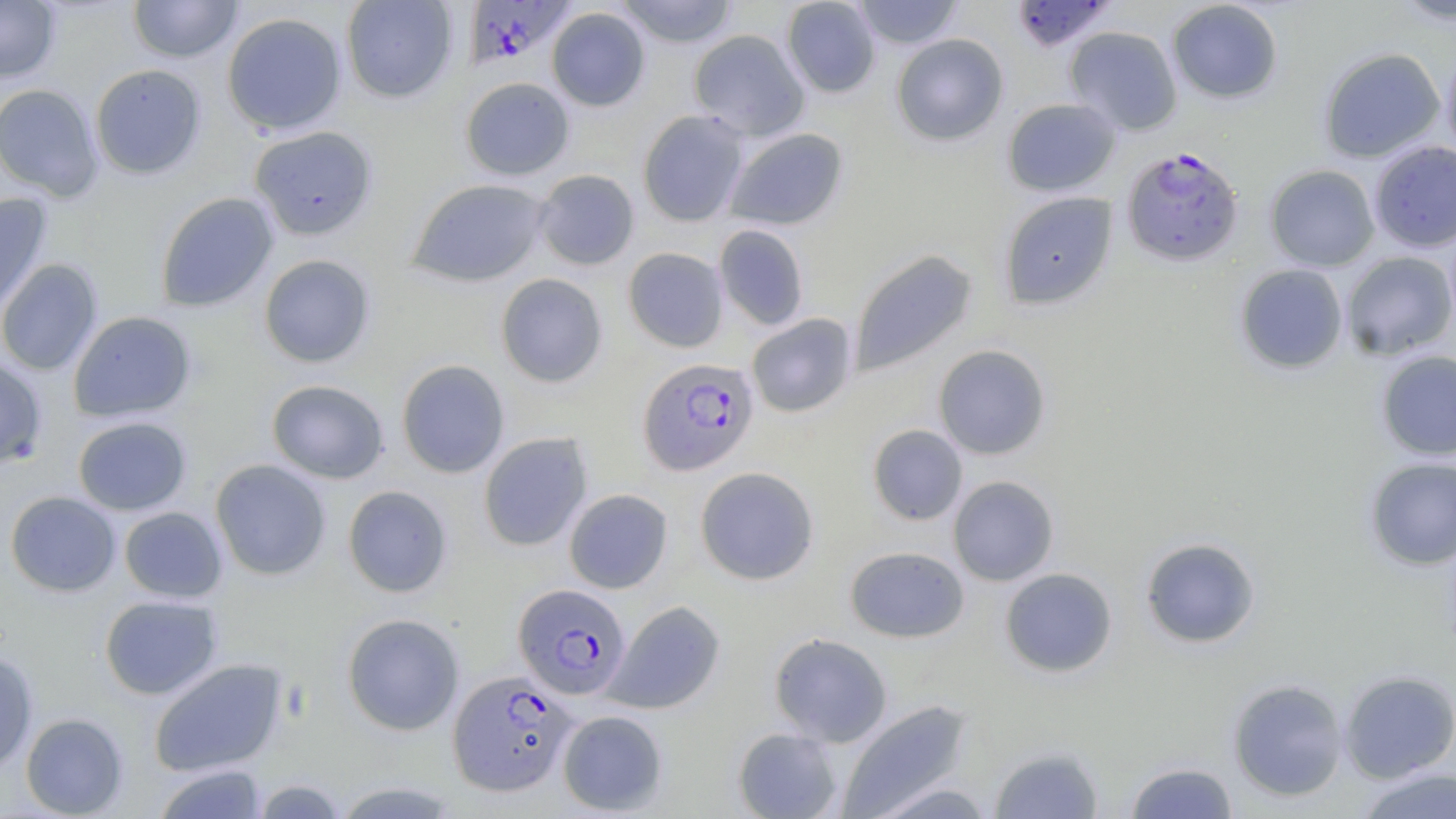
Summary:
  - Coordinate format: approximate bounding boxes as [x1, y1, x2, y2] in pixels
  - Uninfected red blood cell locations: [0, 0, 61, 83], [128, 0, 243, 63], [341, 0, 458, 103], [612, 0, 741, 48], [781, 0, 880, 98], [851, 0, 964, 49], [1167, 0, 1283, 104], [1388, 0, 1455, 27], [547, 7, 650, 111], [222, 12, 347, 136], [1064, 26, 1182, 136], [689, 29, 810, 141], [891, 33, 1008, 146], [1441, 43, 1456, 161], [1318, 47, 1445, 163], [90, 64, 207, 179], [460, 77, 574, 180], [0, 83, 104, 202], [1002, 98, 1121, 197], [637, 109, 750, 227], [248, 125, 378, 241], [724, 127, 848, 231], [1369, 140, 1456, 253], [1264, 164, 1379, 271], [533, 169, 639, 271], [407, 178, 550, 288], [998, 191, 1118, 310], [155, 192, 279, 313], [0, 193, 52, 317], [714, 224, 810, 330], [623, 247, 728, 353], [849, 249, 978, 377], [1341, 251, 1456, 361], [258, 254, 376, 368], [0, 259, 103, 376], [1234, 264, 1348, 375], [495, 273, 609, 388], [68, 311, 196, 422], [746, 313, 857, 418], [933, 344, 1051, 460], [1375, 350, 1456, 461], [0, 355, 48, 469], [396, 359, 510, 478], [266, 379, 389, 484], [72, 416, 192, 516], [867, 424, 968, 526], [478, 432, 593, 552], [1364, 457, 1456, 570], [210, 459, 332, 581], [695, 466, 819, 585], [948, 476, 1059, 586], [343, 485, 453, 597], [564, 489, 673, 594], [5, 491, 121, 597], [119, 507, 228, 603], [1140, 537, 1260, 649], [844, 546, 970, 643], [1000, 567, 1118, 678], [99, 595, 223, 700], [605, 600, 725, 714], [342, 613, 465, 735], [769, 632, 893, 746], [0, 651, 39, 772], [149, 658, 288, 777], [1338, 669, 1456, 783], [1227, 678, 1348, 802], [837, 699, 973, 819], [557, 710, 668, 815], [20, 713, 129, 818], [732, 727, 844, 818], [989, 746, 1104, 819], [1124, 761, 1238, 819], [152, 763, 267, 819], [1355, 767, 1455, 819], [251, 778, 348, 818], [867, 780, 997, 819], [330, 781, 465, 818]
  - Plasmodium falciparum-infected red blood cell locations: [461, 0, 578, 70], [1011, 0, 1117, 52], [1121, 147, 1244, 267], [637, 357, 759, 476], [513, 583, 631, 699], [447, 670, 578, 796]
  - Slide-level diagnosis: Plasmodium falciparum
  - Modality: light microscopy
  - Field of view: one of a larger specimen
  - Magnification: 1000x
  - Preparation: thin blood smear
  - Stain: May-Grünwald-Giemsa
  - Image size: 1456×819 pixels